Assess this cell for malaria.
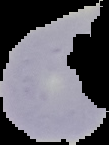
It is uninfected.

image size = 109×145 pixels
image type = segmented cell region with the area outside set to black
preparation = thin blood film